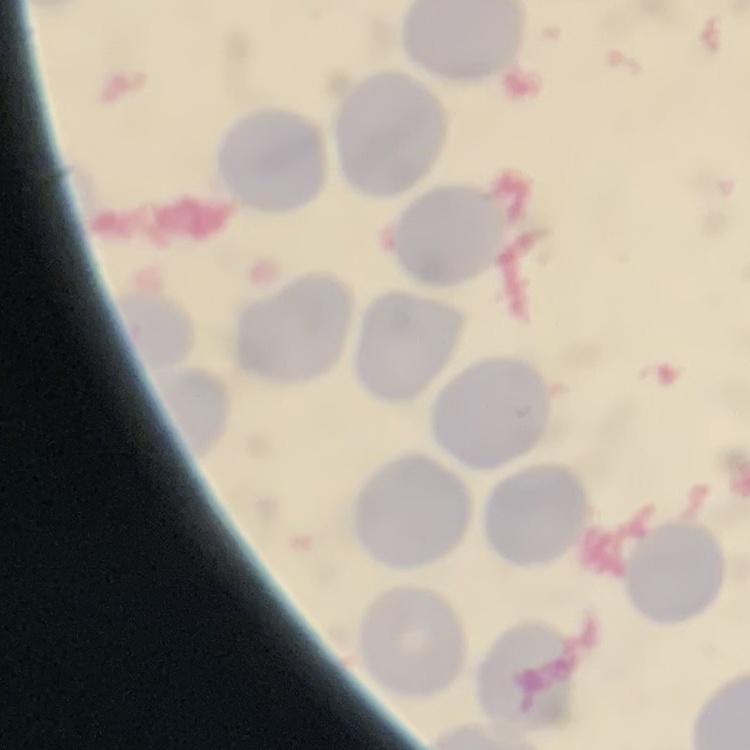

Summary:
  - Erythrocyte morphology: no rouleaux formation
  - Preparation: thin blood film
  - Stain: Field's or Giemsa
  - Image type: one tile cut from a larger photomicrograph